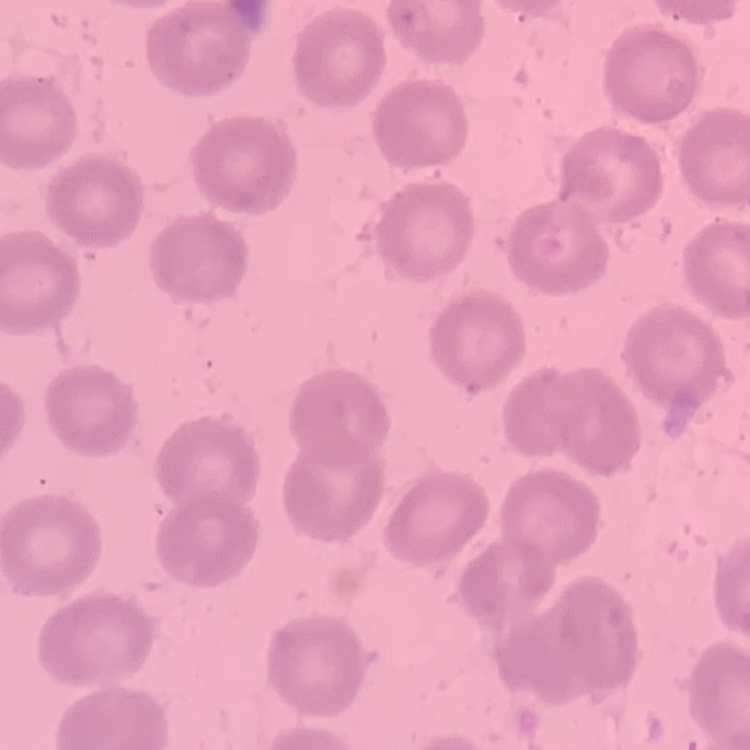
The red blood cells exhibit no rouleaux formation. Field's or Giemsa stain. Square crop of a larger photomicrograph. Thin peripheral smear.